Locate and identify every blood parasite.
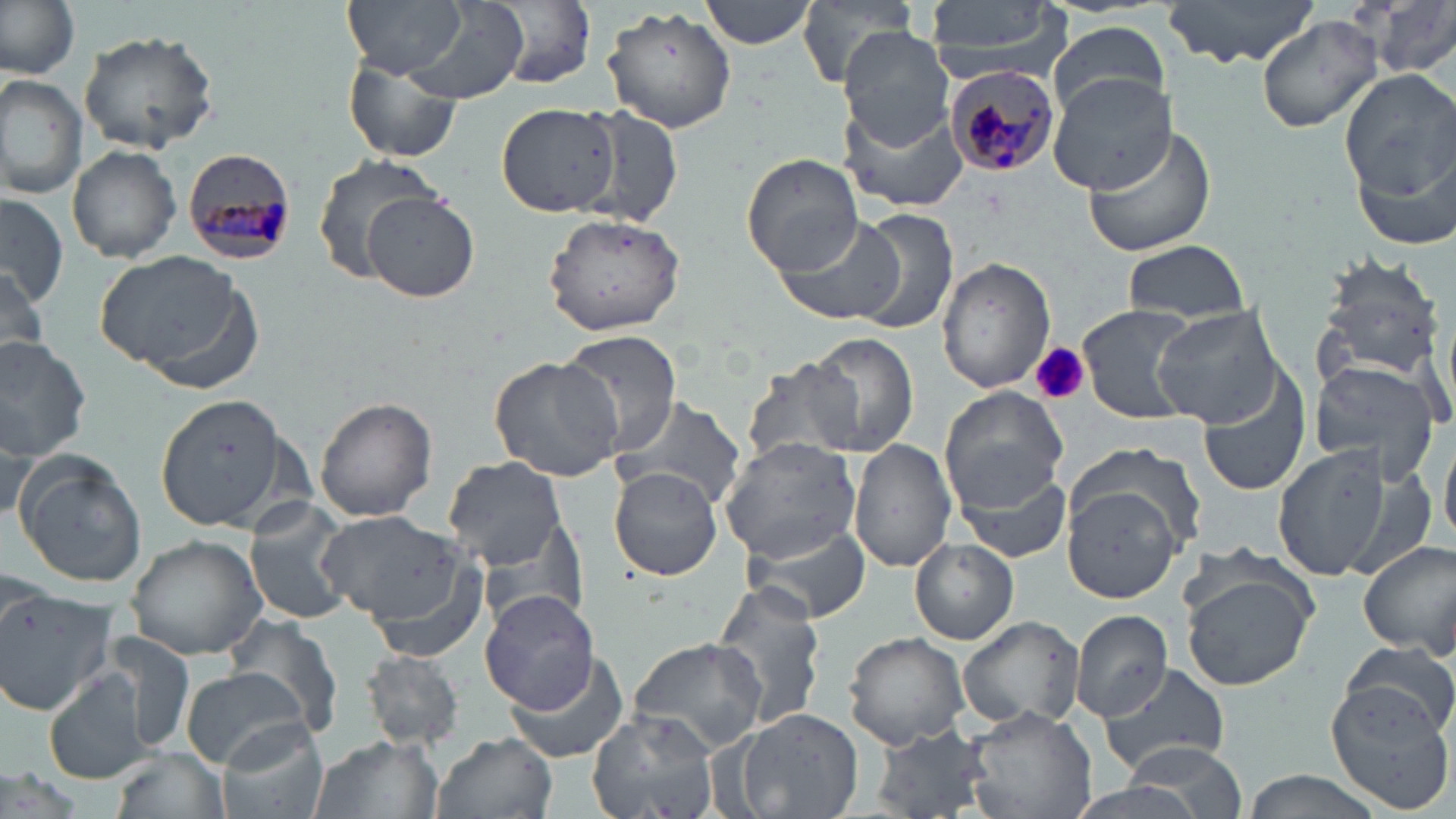

Approximate bounding boxes as (x1,y1)-(x2,y2) corner pairs in pixels.
Plasmodium malariae-infected red blood cells: (943,66)-(1062,179), (181,148)-(300,264).
No Plasmodium falciparum, Plasmodium ovale, Plasmodium vivax, Babesia divergens, or Trypanosoma brucei observed.

Uninfected red blood cell locations: (0,0)-(79,80), (341,0)-(471,78), (480,0)-(597,89), (700,0)-(817,49), (929,0)-(1071,79), (1166,0)-(1317,70), (1362,0)-(1456,78), (797,1)-(916,86), (603,5)-(735,134), (394,8)-(531,108), (1257,14)-(1385,132), (1048,19)-(1171,118), (838,28)-(955,148), (78,30)-(218,154), (345,56)-(465,164), (1337,65)-(1455,210), (0,72)-(87,201), (1048,72)-(1177,193), (841,100)-(965,214), (496,102)-(623,216), (575,102)-(687,230), (1083,126)-(1217,258), (67,143)-(182,264), (311,153)-(444,282), (742,153)-(863,276), (360,191)-(480,303), (0,194)-(69,306), (845,208)-(959,335), (542,211)-(689,337), (773,212)-(905,325), (1123,239)-(1248,322), (95,251)-(252,377), (1312,253)-(1448,386), (937,255)-(1054,394), (0,264)-(48,367), (1077,303)-(1202,424), (1152,305)-(1285,427), (554,329)-(686,454), (799,333)-(921,458), (0,334)-(92,462), (487,355)-(625,481), (1309,357)-(1442,488), (738,360)-(863,469), (1200,363)-(1314,497), (941,387)-(1069,509), (153,393)-(292,533), (609,394)-(745,509), (315,397)-(437,521), (1441,428)-(1456,549), (720,436)-(864,564), (849,438)-(956,573), (1274,439)-(1393,579), (1066,443)-(1207,556), (14,454)-(147,589), (443,456)-(566,567), (608,465)-(723,581), (952,466)-(1072,567), (1063,483)-(1183,605), (244,499)-(357,629), (319,510)-(468,630), (741,517)-(873,625), (124,535)-(268,660), (911,539)-(1018,644), (1357,539)-(1456,661), (360,551)-(494,663), (1179,563)-(1318,691), (710,581)-(829,731), (0,589)-(118,719), (479,590)-(598,713), (2,592)-(115,718), (224,610)-(345,741), (1070,610)-(1175,723), (957,615)-(1087,733), (99,629)-(200,756), (845,631)-(969,750), (628,636)-(767,753), (1341,641)-(1456,748), (357,650)-(467,750), (502,650)-(629,764), (1098,662)-(1232,775), (42,668)-(155,785), (181,669)-(310,768), (1323,676)-(1455,813), (962,703)-(1099,819), (728,707)-(863,819), (585,708)-(720,819), (219,722)-(329,819), (871,727)-(998,817), (306,732)-(443,819), (435,732)-(556,819), (1098,742)-(1252,817), (110,746)-(231,819), (1235,768)-(1395,819). Platelet locations: (1033,341)-(1089,406). Slide-level diagnosis: Plasmodium malariae. Captured at 1000x magnification. Light microscopy. One field of a larger specimen. Thin blood film. Image is 1456×819 pixels. May-Grünwald-Giemsa-stained preparation.